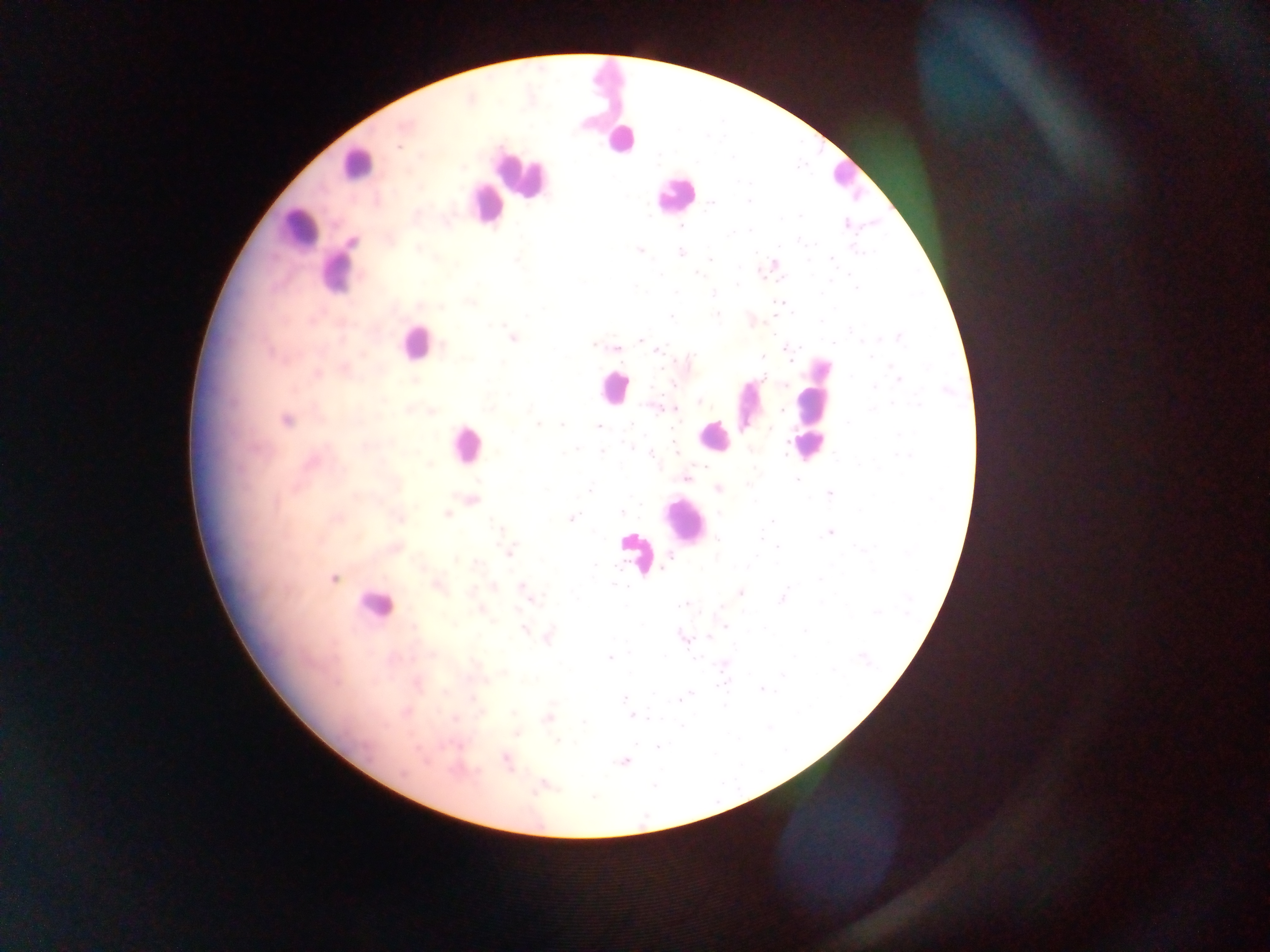
preparation: thick blood smear
image_size: 1270×952 pixels
country: Ghana
capture: mobile-phone photograph through a microscope
field_of_view: single
leukocyte_locations: 'approximate centers as [x, y] in pixels: [604, 92], [620, 140], [355, 163], [519, 174], [843, 174], [672, 192], [486, 201], [296, 230], [336, 274], [414, 343], [614, 386], [747, 406], [808, 417], [714, 437], [465, 445], [682, 519], [636, 552], [373, 604]'
plasmodium_parasite_locations: 'approximate centers as [x, y] in pixels: [406, 125], [399, 146], [464, 168], [748, 201], [712, 203], [800, 215], [846, 224], [681, 226], [749, 231], [814, 244], [418, 249], [639, 251], [755, 251], [859, 252], [680, 253], [710, 259], [832, 259], [517, 260], [808, 260], [774, 263], [760, 272], [698, 274], [660, 275], [781, 279], [738, 285], [635, 288], [856, 288], [676, 293], [713, 294], [471, 302], [441, 306], [792, 312], [717, 315], [670, 316], [851, 330], [512, 338], [899, 338], [878, 339], [640, 341], [834, 342], [443, 345], [594, 345], [617, 348], [799, 348], [658, 350], [762, 357], [789, 357], [871, 357], [689, 360], [764, 377], [899, 378], [673, 385], [652, 387], [874, 387], [947, 391], [701, 402], [892, 403], [919, 405], [660, 409], [781, 409], [873, 410], [286, 420], [848, 423], [537, 424], [562, 426], [599, 427], [770, 429], [900, 435], [786, 443], [629, 446], [674, 446], [573, 451], [602, 451], [903, 454], [651, 455], [785, 455], [703, 466], [686, 478], [796, 479], [748, 485], [718, 489], [589, 491], [829, 493], [472, 499], [641, 505], [446, 513], [623, 513], [720, 513], [571, 518], [771, 521], [830, 532], [761, 539], [719, 541], [778, 547], [509, 551], [671, 558], [476, 563], [595, 564], [820, 579], [615, 585], [438, 586], [493, 586], [523, 587], [739, 592], [528, 596], [782, 597], [685, 604], [722, 606], [480, 609], [876, 612], [725, 626], [764, 628], [524, 630], [549, 636], [683, 636], [709, 636], [610, 657], [664, 657], [863, 657], [834, 670], [783, 674], [417, 684], [761, 689], [625, 699], [681, 699], [515, 713], [632, 716], [548, 717], [518, 733], [557, 740], [658, 746], [506, 761], [624, 762], [542, 786]'